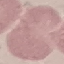

malaria_status: uninfected
preparation: thin blood film
capture: smartphone through the microscope eyepiece
image_type: automatically extracted cell patch, resized to 64 × 64 pixels
stain: Giemsa